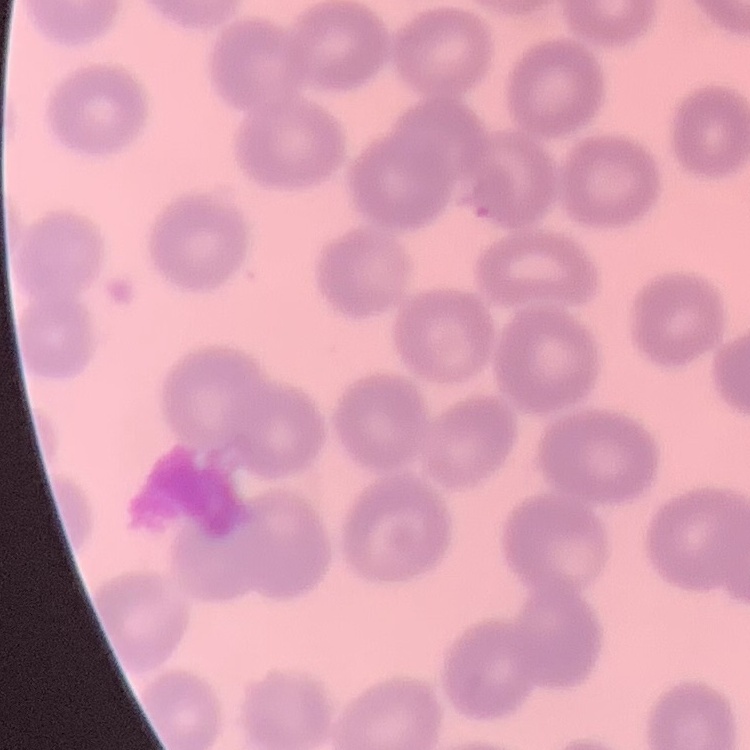
Summary:
  - Erythrocyte morphology: no rouleaux formation
  - Stain: Field's or Giemsa
  - Preparation: thin blood smear
  - Image type: one tile cut from a larger photomicrograph